Locate every blood parasite and identify its species.
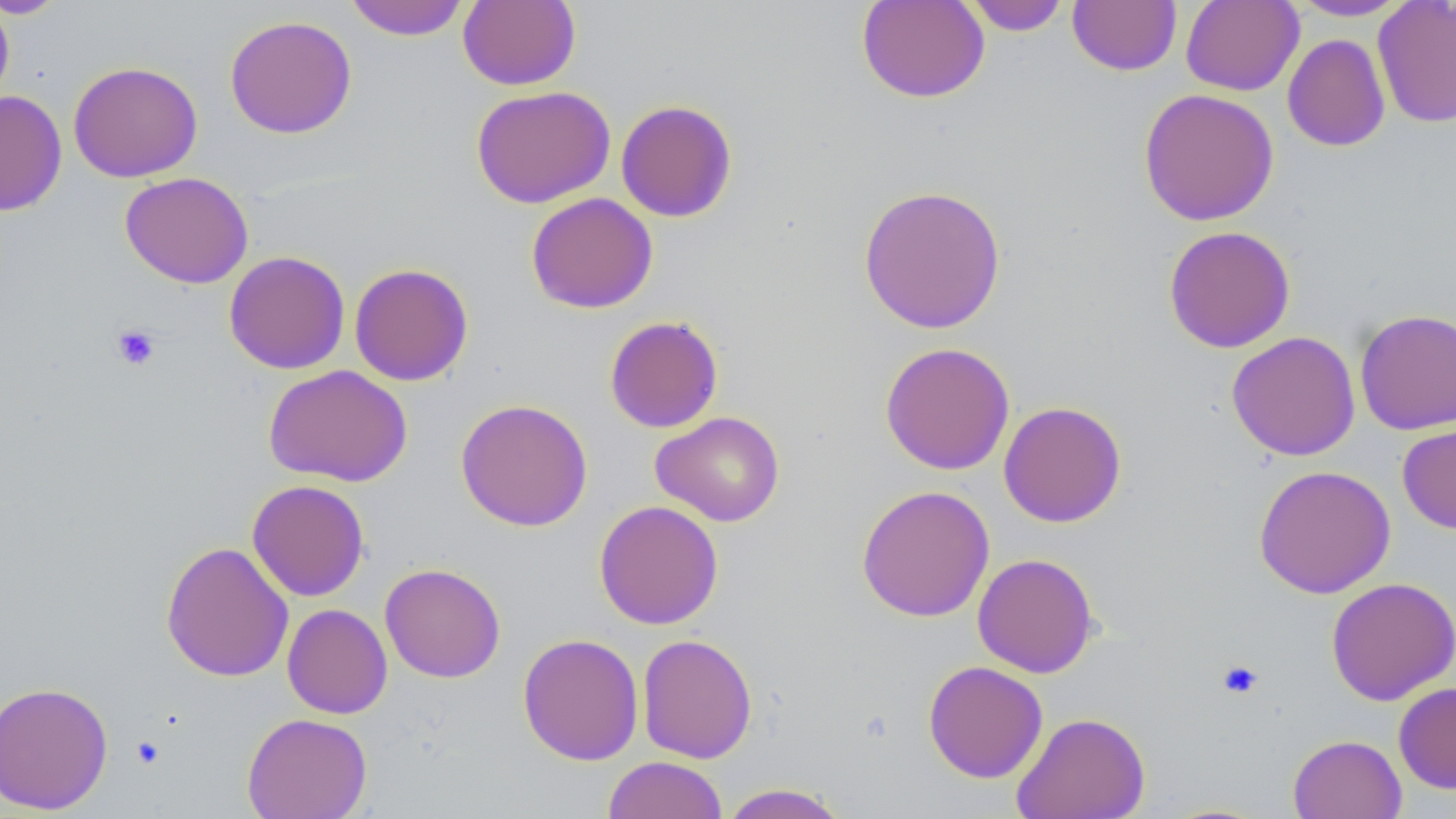
No blood parasites observed.

Summary:
  - Coordinate format: approximate bounding boxes as (x1, y1, x2, y2) in pixels
  - Platelet locations: (111, 323, 161, 371), (1216, 659, 1265, 700), (131, 735, 166, 769)
  - Uninfected red blood cell locations: (0, 0, 69, 19), (344, 0, 471, 41), (458, 0, 581, 91), (856, 0, 990, 103), (962, 0, 1072, 36), (1180, 0, 1304, 96), (1285, 0, 1416, 21), (0, 1, 14, 109), (1067, 1, 1182, 76), (1372, 1, 1456, 129), (224, 14, 357, 139), (1282, 34, 1391, 152), (68, 61, 203, 182), (470, 85, 615, 208), (1137, 88, 1279, 226), (0, 91, 67, 216), (615, 99, 738, 223), (119, 171, 254, 289), (857, 184, 1007, 335), (525, 192, 658, 314), (1162, 225, 1296, 353), (223, 250, 350, 374), (349, 263, 474, 386), (1354, 308, 1456, 435), (604, 315, 724, 433), (1226, 331, 1361, 461), (879, 341, 1015, 475), (263, 364, 413, 486), (455, 398, 593, 532), (998, 401, 1127, 528), (650, 411, 785, 527), (1397, 420, 1456, 535), (1253, 464, 1396, 598), (246, 479, 370, 601), (856, 485, 995, 622), (593, 500, 724, 630), (160, 540, 294, 682), (972, 552, 1099, 678), (380, 562, 506, 683), (1325, 576, 1456, 706), (281, 603, 393, 719), (517, 632, 644, 765), (636, 633, 758, 763), (923, 660, 1048, 783), (0, 680, 114, 815), (1393, 682, 1456, 794), (1011, 711, 1150, 819), (242, 712, 372, 819), (1288, 734, 1407, 819), (602, 756, 728, 819), (719, 783, 850, 819)
  - Slide-level diagnosis: negative for blood parasites
  - Stain: May-Grünwald-Giemsa
  - Preparation: thin blood film
  - Modality: light microscopy
  - Magnification: 1000x
  - Field of view: one of a larger specimen
  - Image size: 1456×819 pixels